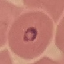

Malaria status: parasitized. Giemsa-stained preparation. Automatically extracted cell patch, resized to 64 × 64 pixels. Acquired by smartphone through the microscope eyepiece. Thin smear of blood.